Give the position of every malaria parasite and every leukocyte.
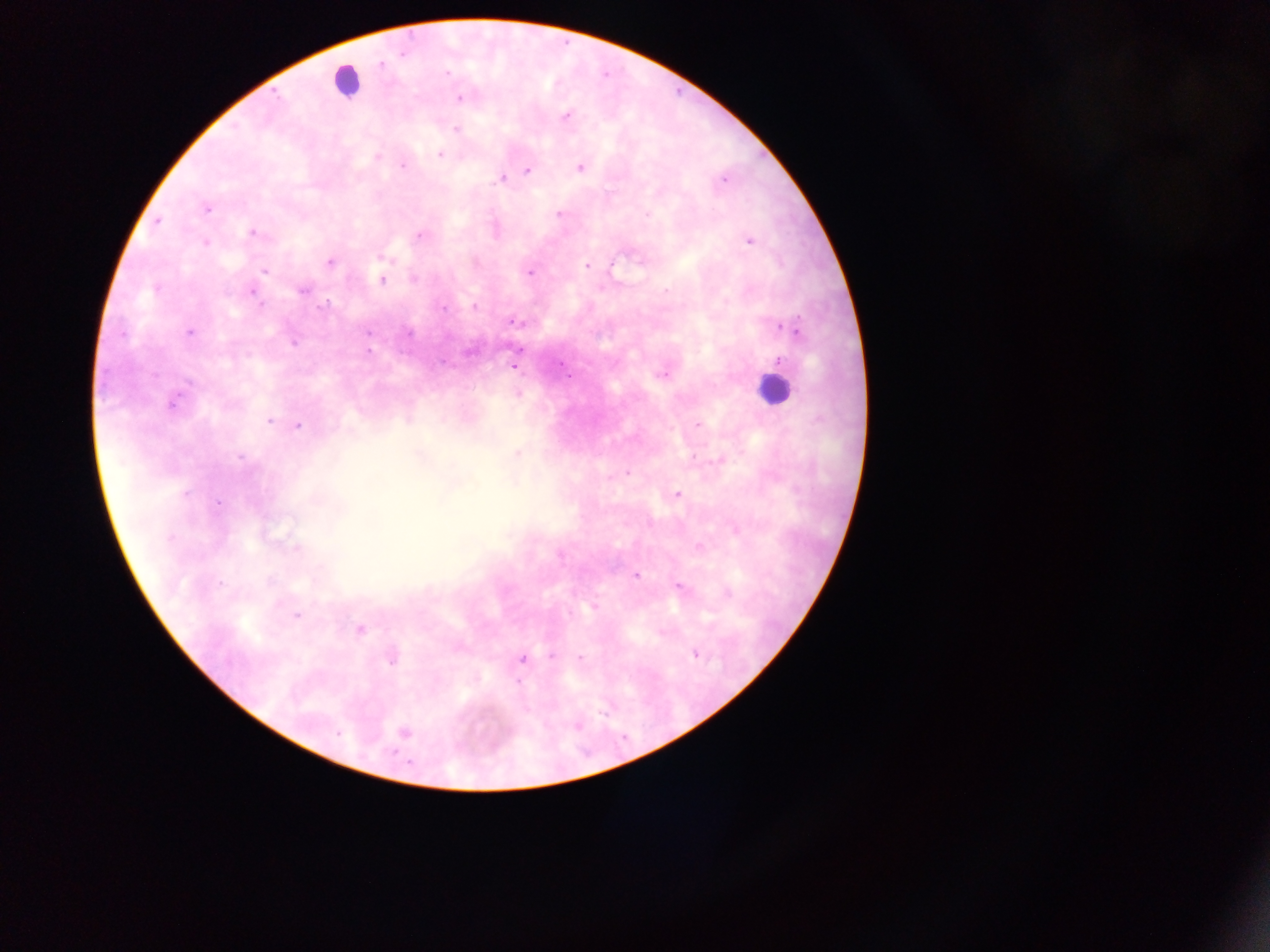
Approximate centers as x y in pixels.
Malaria parasites: 402 53; 381 64; 447 72; 459 98; 566 116; 456 130; 439 155; 377 158; 403 166; 580 167; 528 170; 500 179; 724 179; 207 208; 561 214; 156 222; 252 232; 420 236; 750 241; 205 243; 381 258; 330 263; 612 264; 586 266; 264 271; 529 272; 413 279; 382 280; 155 289; 302 290; 666 291; 252 292; 259 303; 326 305; 475 307; 443 309; 516 323; 789 329; 189 332; 409 332; 122 333; 368 333; 293 342; 368 351; 779 361; 515 366; 663 374; 190 382; 172 403; 269 421; 698 425; 297 426; 517 453; 240 457; 627 472; 186 493; 677 494; 219 502; 735 529; 296 548; 699 548; 559 556; 636 576; 220 583; 679 587; 728 594; 594 607; 297 616; 360 628; 695 654; 551 656; 580 658; 392 660; 522 660; 518 682; 338 733; 404 733.
Leukocytes: 346 81; 772 390.

Mobile-phone photograph taken through the microscope. Image is 1270×952 pixels. Thick blood film. Single field of view. Sample from Ghana.